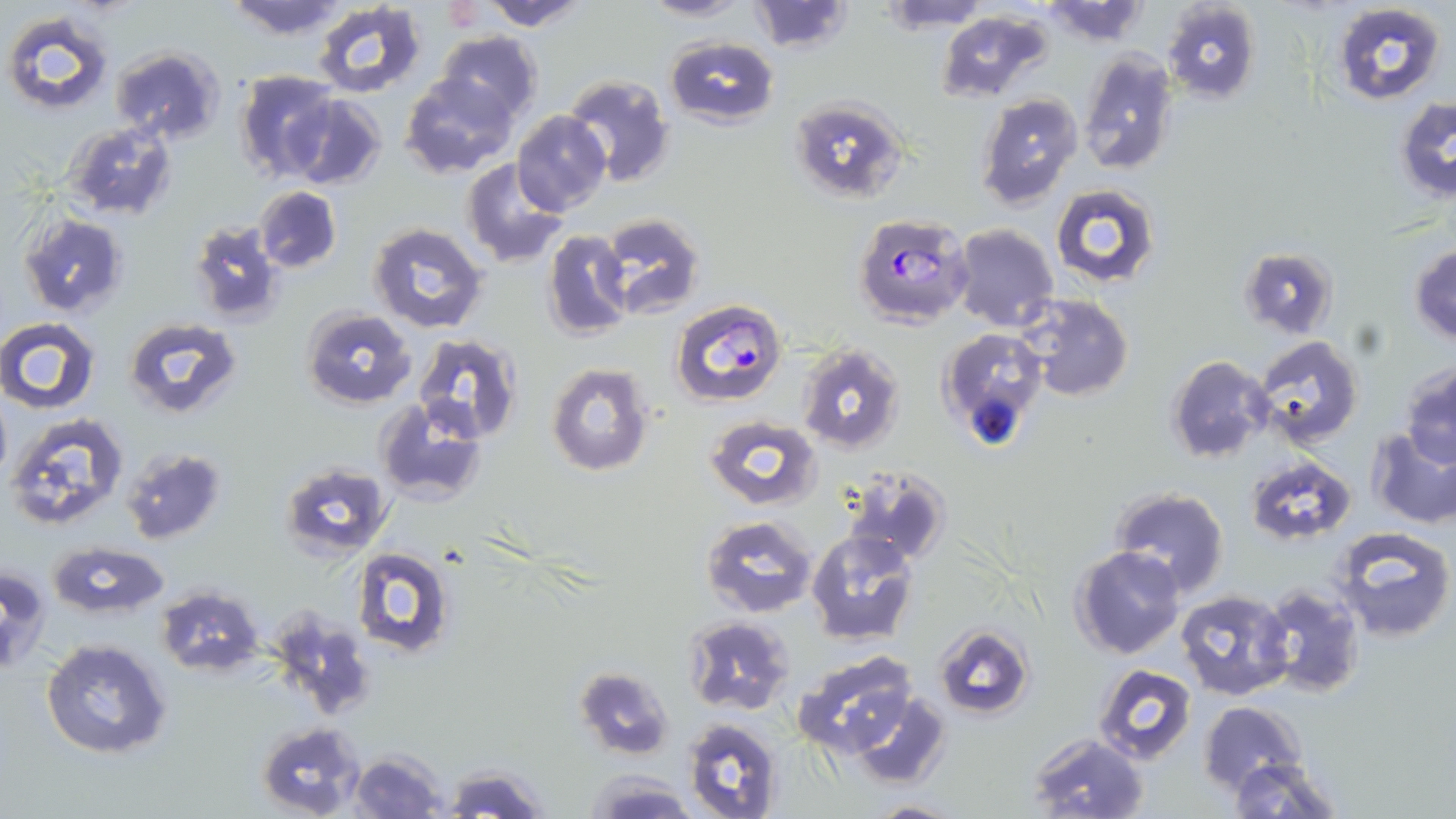
slide_level_diagnosis: Plasmodium falciparum
magnification: 1000x
image_size: 1456×819 pixels
stain: May-Grünwald-Giemsa
modality: optical microscopy
uninfected_red_blood_cell_locations: 'approximate bounding boxes as (x1, y1, x2, y2) in pixels: (222, 0, 351, 41), (479, 0, 591, 29), (639, 0, 751, 22), (747, 0, 854, 52), (878, 0, 992, 30), (1160, 0, 1262, 104), (311, 1, 429, 97), (1331, 1, 1445, 106), (1041, 2, 1150, 45), (1, 9, 115, 116), (935, 9, 1057, 106), (434, 31, 542, 124), (664, 35, 781, 128), (111, 46, 226, 146), (1078, 47, 1179, 176), (234, 70, 341, 182), (401, 72, 519, 178), (561, 74, 674, 188), (1016, 89, 1150, 205), (975, 91, 1083, 208), (287, 94, 386, 190), (790, 95, 906, 200), (1394, 97, 1456, 202), (512, 111, 611, 215), (63, 121, 180, 221), (460, 158, 569, 268), (1051, 184, 1160, 290), (255, 186, 342, 272), (596, 214, 706, 317), (18, 215, 130, 317), (188, 216, 285, 324), (367, 221, 489, 334), (951, 223, 1058, 331), (544, 230, 634, 340), (1410, 243, 1456, 344), (1241, 247, 1336, 337), (1018, 295, 1133, 402), (302, 307, 416, 408), (123, 317, 243, 419), (1, 318, 101, 413), (937, 326, 1049, 449), (411, 333, 525, 446), (1252, 334, 1365, 450), (796, 344, 905, 456), (1167, 355, 1273, 461), (1399, 361, 1456, 468), (547, 364, 653, 477), (0, 394, 11, 483), (372, 398, 487, 505), (3, 412, 129, 532), (703, 414, 823, 512), (1365, 426, 1456, 528), (120, 448, 227, 543), (1245, 453, 1356, 546), (279, 463, 393, 562), (842, 467, 951, 566), (1109, 488, 1229, 598), (700, 513, 817, 617), (1329, 524, 1456, 642), (805, 529, 917, 645), (48, 542, 167, 618), (1070, 546, 1185, 661), (351, 547, 457, 661), (0, 565, 51, 673), (1259, 583, 1365, 698), (154, 585, 266, 676), (1175, 588, 1295, 700), (269, 607, 377, 723), (684, 616, 794, 714), (933, 623, 1035, 722), (41, 637, 172, 759), (791, 650, 920, 756), (1090, 663, 1197, 766), (573, 665, 675, 762), (845, 689, 954, 790), (1200, 700, 1306, 795), (681, 716, 785, 819), (256, 721, 367, 818), (1025, 732, 1150, 819), (351, 751, 450, 819), (1224, 756, 1344, 819), (442, 762, 548, 819), (584, 771, 696, 818), (864, 798, 963, 818)'
preparation: thin blood smear
plasmodium_falciparum_infected_red_blood_cell_locations: 'approximate bounding boxes as (x1, y1, x2, y2) in pixels: (853, 213, 975, 329), (670, 299, 786, 407)'
field_of_view: one of a larger specimen
platelet_locations: 'approximate bounding boxes as (x1, y1, x2, y2) in pixels: (440, 1, 487, 31)'